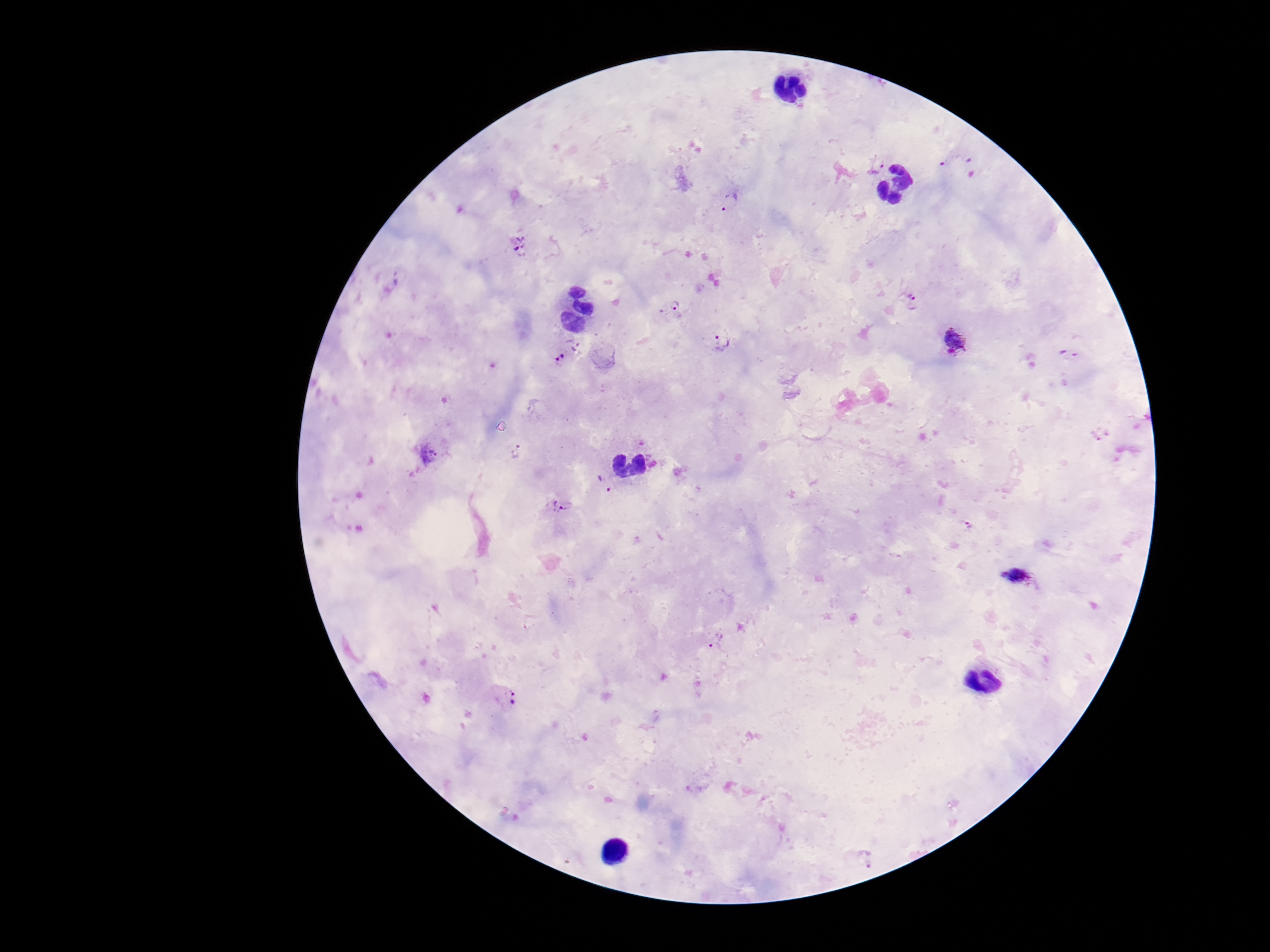 Approximate object centers, in pixels from the top-left corner. Plasmodium parasite locations: (x=956, y=160), (x=877, y=165), (x=729, y=201), (x=520, y=243), (x=398, y=278), (x=911, y=302), (x=675, y=305), (x=723, y=341), (x=956, y=342), (x=1068, y=354), (x=563, y=356), (x=517, y=451), (x=428, y=454), (x=604, y=484), (x=563, y=506), (x=1022, y=578), (x=716, y=638), (x=507, y=696), (x=866, y=860). 100x magnification. Patient malaria status: positive. Giemsa stain. Smartphone photograph taken through the microscope eyepiece. Thick blood smear. Single field of view. Image is 1270×952 pixels.